State which cell type is depicted.
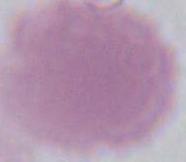
An erythrocyte.

modality: micrograph
magnification: 1000x